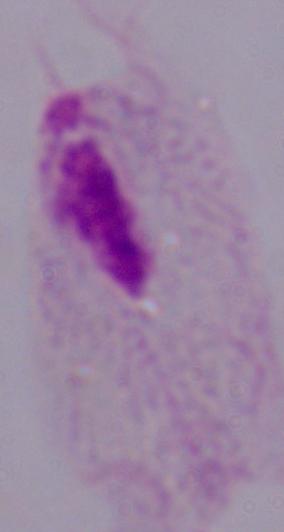

Summary:
  - Identification: trichomonad
  - Magnification: 1000x
  - Modality: photomicrograph